State the blood parasite species.
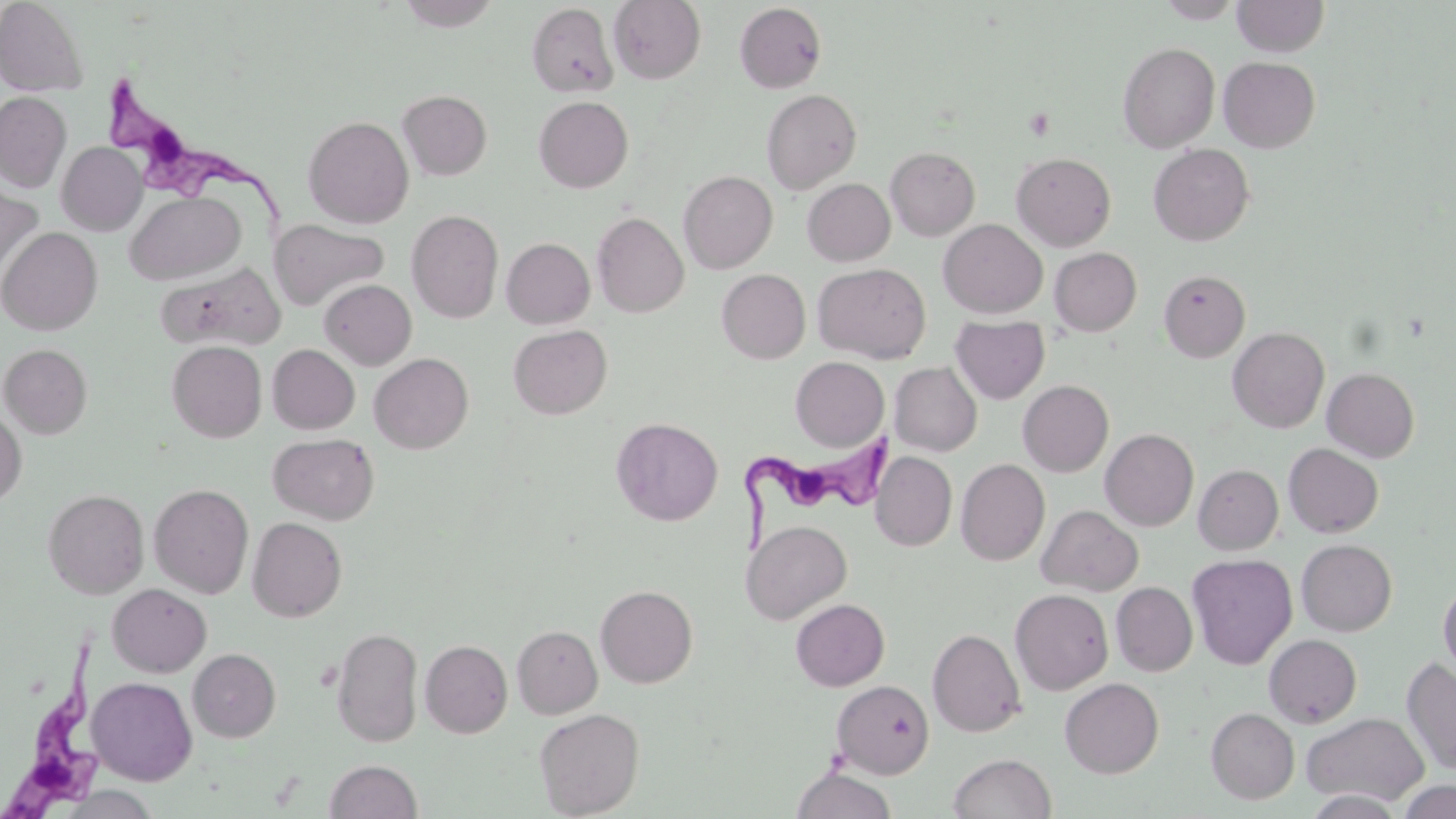

Trypanosoma brucei.

Approximate bounding boxes as named x1/y1/x2/y2 corners in pixels. Platelet locations: (x1=1023, y1=107, x2=1055, y2=141). Uninfected red blood cell locations: (x1=0, y1=0, x2=88, y2=96), (x1=607, y1=0, x2=706, y2=84), (x1=1156, y1=0, x2=1244, y2=23), (x1=1233, y1=0, x2=1329, y2=57), (x1=394, y1=1, x2=502, y2=31), (x1=526, y1=3, x2=619, y2=97), (x1=734, y1=3, x2=827, y2=93), (x1=1118, y1=42, x2=1220, y2=153), (x1=1218, y1=56, x2=1320, y2=153), (x1=761, y1=89, x2=862, y2=194), (x1=397, y1=90, x2=493, y2=180), (x1=0, y1=92, x2=71, y2=192), (x1=533, y1=96, x2=633, y2=192), (x1=303, y1=116, x2=414, y2=228), (x1=57, y1=142, x2=147, y2=235), (x1=1148, y1=144, x2=1254, y2=246), (x1=885, y1=147, x2=980, y2=240), (x1=1011, y1=152, x2=1116, y2=251), (x1=678, y1=171, x2=778, y2=273), (x1=803, y1=178, x2=895, y2=266), (x1=0, y1=184, x2=43, y2=279), (x1=125, y1=190, x2=245, y2=285), (x1=407, y1=210, x2=503, y2=323), (x1=592, y1=212, x2=689, y2=318), (x1=270, y1=219, x2=388, y2=311), (x1=938, y1=219, x2=1048, y2=319), (x1=0, y1=227, x2=102, y2=335), (x1=501, y1=238, x2=595, y2=329), (x1=1050, y1=247, x2=1141, y2=336), (x1=813, y1=263, x2=931, y2=363), (x1=156, y1=264, x2=285, y2=351), (x1=717, y1=269, x2=810, y2=363), (x1=1159, y1=270, x2=1250, y2=362), (x1=319, y1=279, x2=416, y2=369), (x1=950, y1=316, x2=1050, y2=403), (x1=508, y1=324, x2=612, y2=419), (x1=1227, y1=326, x2=1329, y2=433), (x1=166, y1=341, x2=267, y2=442), (x1=1, y1=344, x2=93, y2=438), (x1=267, y1=344, x2=359, y2=434), (x1=369, y1=353, x2=473, y2=454), (x1=791, y1=357, x2=889, y2=451), (x1=883, y1=360, x2=969, y2=551), (x1=890, y1=362, x2=982, y2=456), (x1=1322, y1=367, x2=1419, y2=462), (x1=1018, y1=380, x2=1114, y2=477), (x1=0, y1=409, x2=27, y2=507), (x1=611, y1=417, x2=723, y2=526), (x1=1100, y1=429, x2=1199, y2=531), (x1=268, y1=433, x2=379, y2=524), (x1=1283, y1=443, x2=1383, y2=538), (x1=872, y1=452, x2=957, y2=550), (x1=956, y1=459, x2=1050, y2=566), (x1=1193, y1=464, x2=1283, y2=554), (x1=149, y1=483, x2=254, y2=598), (x1=42, y1=489, x2=150, y2=598), (x1=1036, y1=505, x2=1143, y2=596), (x1=247, y1=517, x2=347, y2=621), (x1=741, y1=520, x2=852, y2=624), (x1=1296, y1=539, x2=1397, y2=636), (x1=1187, y1=553, x2=1298, y2=670), (x1=1438, y1=580, x2=1456, y2=681), (x1=1111, y1=582, x2=1198, y2=676), (x1=108, y1=584, x2=211, y2=678), (x1=595, y1=585, x2=698, y2=688), (x1=1010, y1=589, x2=1113, y2=694), (x1=791, y1=598, x2=889, y2=690), (x1=512, y1=625, x2=603, y2=718), (x1=331, y1=627, x2=424, y2=748), (x1=927, y1=628, x2=1026, y2=737), (x1=1264, y1=634, x2=1362, y2=728), (x1=420, y1=639, x2=513, y2=737), (x1=188, y1=648, x2=281, y2=742), (x1=1402, y1=657, x2=1456, y2=777), (x1=86, y1=676, x2=198, y2=785), (x1=1060, y1=677, x2=1163, y2=778), (x1=832, y1=680, x2=935, y2=778), (x1=1206, y1=707, x2=1300, y2=804), (x1=534, y1=708, x2=644, y2=818), (x1=1301, y1=711, x2=1429, y2=807), (x1=948, y1=753, x2=1056, y2=819), (x1=324, y1=759, x2=422, y2=818), (x1=791, y1=767, x2=897, y2=819), (x1=1397, y1=778, x2=1456, y2=818), (x1=54, y1=787, x2=162, y2=819), (x1=1302, y1=791, x2=1407, y2=818). Trypanosoma brucei locations: (x1=110, y1=73, x2=288, y2=222), (x1=745, y1=428, x2=908, y2=558), (x1=1, y1=639, x2=106, y2=818). Image is 1456×819 pixels. One field of a larger specimen. 1000x magnification. Optical microscopy. Thin blood film. May-Grünwald-Giemsa stain.